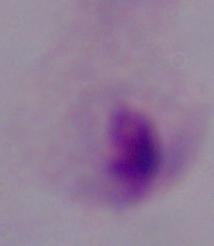

A trichomonad is seen. Photomicrograph. 1000x magnification.